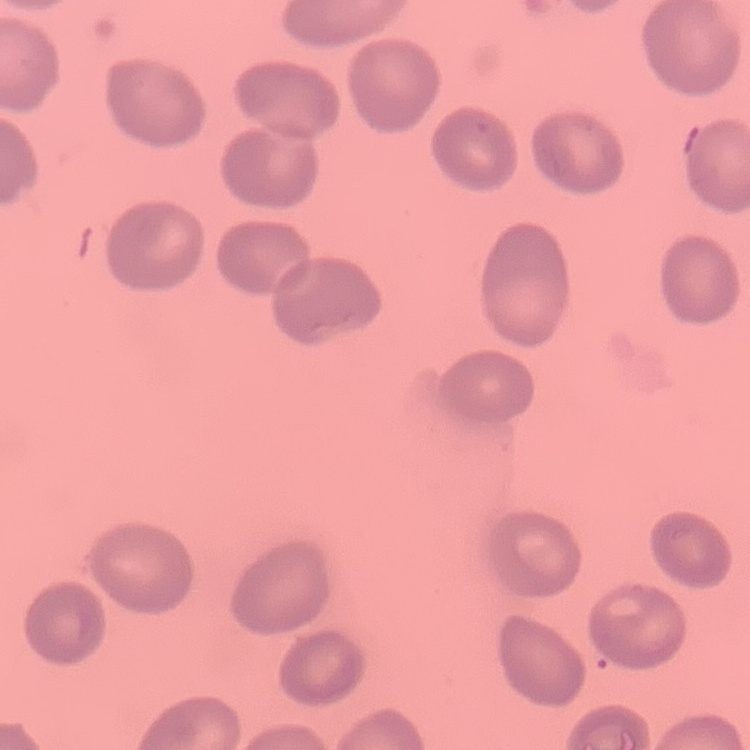 The erythrocytes exhibit no rouleaux formation. Field's or Giemsa stain. Thin blood film. One tile cut from a larger photomicrograph.